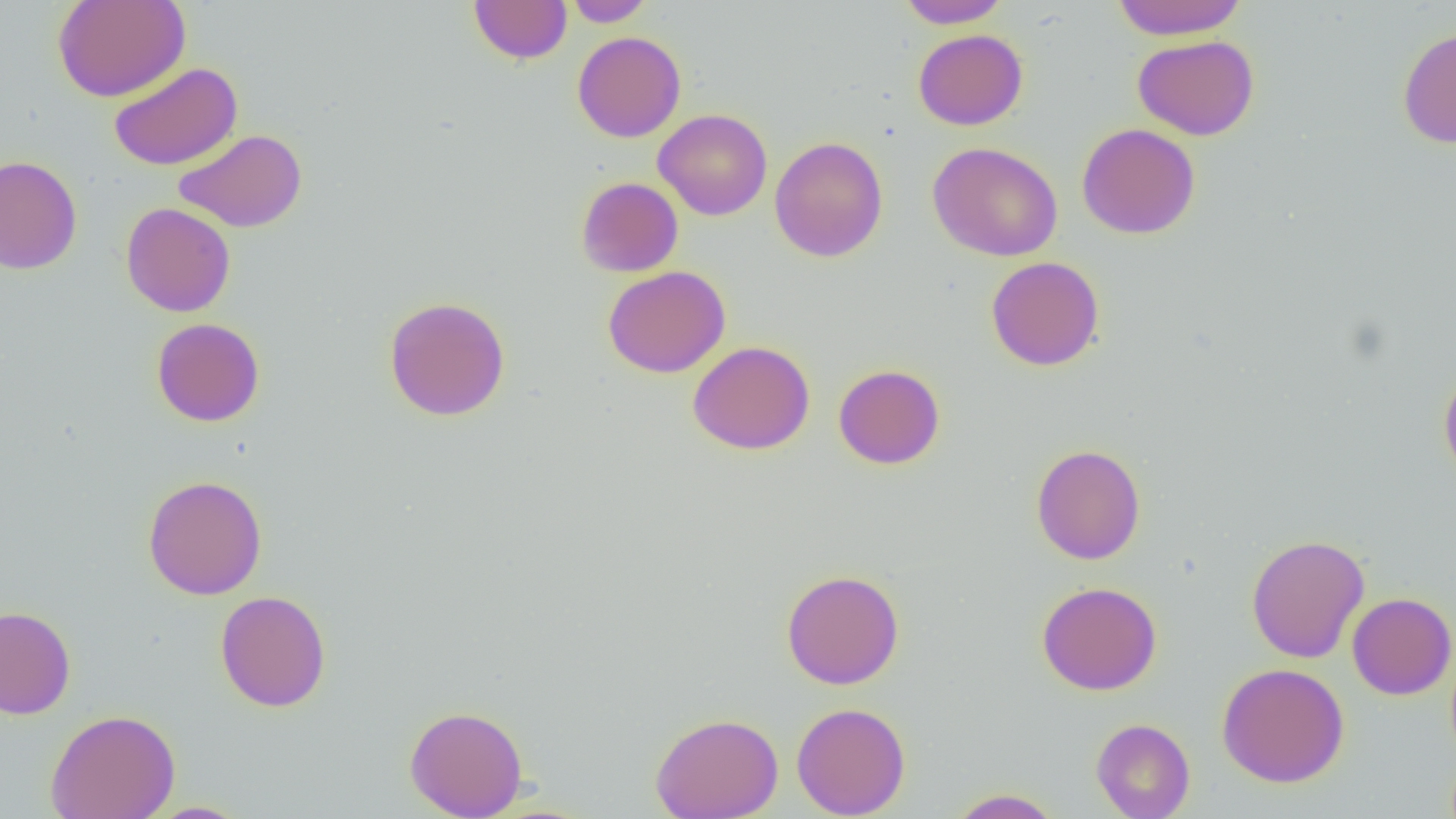

Approximate bounding boxes as named x1/y1/x2/y2 corners in pixels. Uninfected red blood cell locations: (x1=52, y1=0, x2=191, y2=102), (x1=468, y1=0, x2=572, y2=65), (x1=565, y1=0, x2=655, y2=27), (x1=895, y1=0, x2=1012, y2=28), (x1=1111, y1=0, x2=1248, y2=40), (x1=1397, y1=26, x2=1456, y2=149), (x1=913, y1=29, x2=1028, y2=130), (x1=572, y1=31, x2=687, y2=143), (x1=1132, y1=35, x2=1260, y2=140), (x1=108, y1=62, x2=242, y2=170), (x1=653, y1=109, x2=773, y2=221), (x1=1076, y1=123, x2=1201, y2=239), (x1=173, y1=128, x2=307, y2=232), (x1=769, y1=136, x2=888, y2=262), (x1=927, y1=141, x2=1064, y2=261), (x1=0, y1=155, x2=82, y2=275), (x1=576, y1=177, x2=683, y2=277), (x1=121, y1=202, x2=236, y2=317), (x1=986, y1=256, x2=1105, y2=371), (x1=603, y1=266, x2=731, y2=378), (x1=383, y1=295, x2=511, y2=421), (x1=151, y1=318, x2=265, y2=427), (x1=687, y1=340, x2=815, y2=455), (x1=833, y1=364, x2=945, y2=469), (x1=1439, y1=367, x2=1456, y2=488), (x1=1030, y1=443, x2=1146, y2=565), (x1=142, y1=475, x2=268, y2=600), (x1=1246, y1=533, x2=1370, y2=663), (x1=780, y1=569, x2=905, y2=689), (x1=1036, y1=581, x2=1163, y2=696), (x1=214, y1=590, x2=331, y2=712), (x1=1347, y1=592, x2=1456, y2=700), (x1=0, y1=606, x2=76, y2=719), (x1=1216, y1=663, x2=1350, y2=787), (x1=791, y1=702, x2=911, y2=818), (x1=404, y1=704, x2=528, y2=818), (x1=45, y1=709, x2=181, y2=819), (x1=650, y1=712, x2=784, y2=819), (x1=1091, y1=718, x2=1195, y2=819), (x1=946, y1=788, x2=1064, y2=818), (x1=142, y1=801, x2=253, y2=818). Slide-level diagnosis: no evidence of blood parasites. Thin blood smear. Light microscopy. Captured at 1000x magnification. Single field of view. Image is 1456×819 pixels.